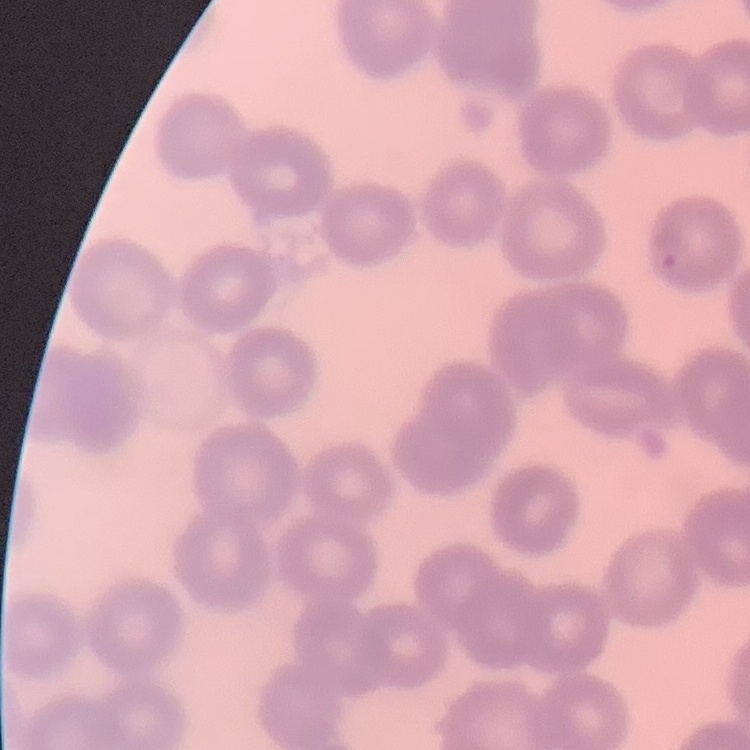
Summary:
  - Red blood cell morphology: no rouleaux formation
  - Image type: square crop of a larger photomicrograph
  - Preparation: thin blood smear
  - Stain: Field's or Giemsa